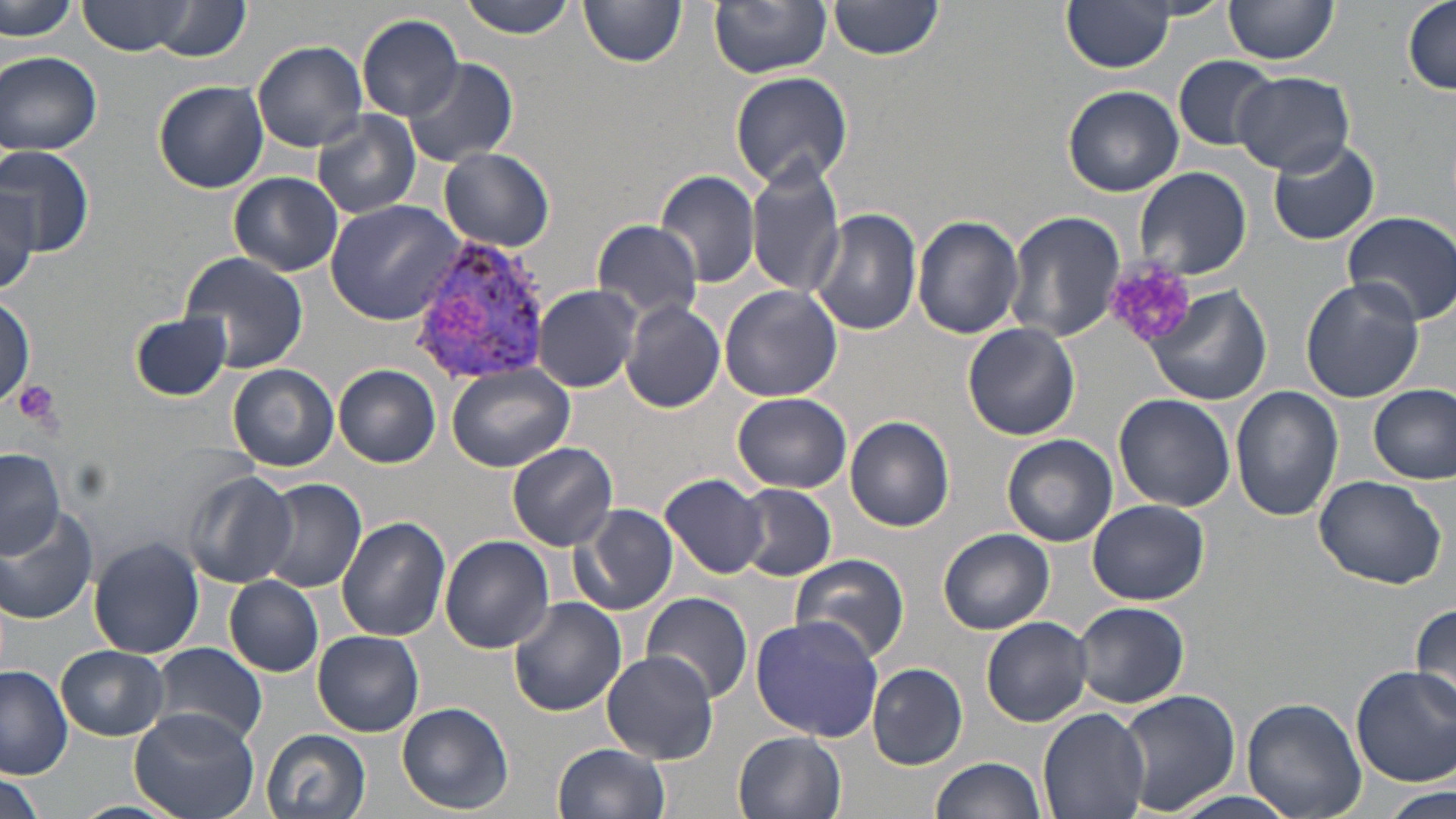

Summary:
  - Coordinate format: approximate bounding boxes as named x1/y1/x2/y2 corners in pixels
  - Uninfected red blood cell locations: (x1=79, y1=0, x2=197, y2=55), (x1=460, y1=0, x2=581, y2=40), (x1=827, y1=0, x2=946, y2=59), (x1=1063, y1=0, x2=1173, y2=72), (x1=1404, y1=0, x2=1456, y2=97), (x1=579, y1=1, x2=686, y2=69), (x1=709, y1=1, x2=831, y2=77), (x1=1222, y1=1, x2=1340, y2=67), (x1=3, y1=2, x2=77, y2=46), (x1=143, y1=2, x2=251, y2=62), (x1=358, y1=14, x2=465, y2=120), (x1=253, y1=40, x2=369, y2=151), (x1=0, y1=51, x2=101, y2=157), (x1=1173, y1=54, x2=1277, y2=152), (x1=401, y1=58, x2=518, y2=169), (x1=730, y1=70, x2=854, y2=190), (x1=1234, y1=72, x2=1355, y2=175), (x1=153, y1=80, x2=269, y2=193), (x1=1063, y1=85, x2=1183, y2=196), (x1=313, y1=113, x2=422, y2=219), (x1=1268, y1=138, x2=1380, y2=245), (x1=0, y1=145, x2=96, y2=257), (x1=440, y1=147, x2=556, y2=252), (x1=747, y1=155, x2=845, y2=298), (x1=1134, y1=166, x2=1251, y2=279), (x1=656, y1=169, x2=759, y2=288), (x1=227, y1=172, x2=343, y2=276), (x1=0, y1=181, x2=42, y2=291), (x1=324, y1=197, x2=468, y2=323), (x1=1006, y1=207, x2=1127, y2=344), (x1=810, y1=208, x2=922, y2=336), (x1=1341, y1=210, x2=1456, y2=326), (x1=915, y1=215, x2=1024, y2=338), (x1=593, y1=219, x2=703, y2=321), (x1=181, y1=252, x2=308, y2=373), (x1=1301, y1=278, x2=1426, y2=404), (x1=534, y1=283, x2=642, y2=392), (x1=718, y1=283, x2=843, y2=402), (x1=1145, y1=283, x2=1273, y2=407), (x1=0, y1=296, x2=34, y2=406), (x1=621, y1=300, x2=725, y2=412), (x1=133, y1=313, x2=231, y2=400), (x1=963, y1=323, x2=1079, y2=440), (x1=228, y1=364, x2=339, y2=471), (x1=335, y1=364, x2=441, y2=468), (x1=446, y1=367, x2=574, y2=473), (x1=1370, y1=385, x2=1454, y2=484), (x1=1230, y1=386, x2=1343, y2=522), (x1=732, y1=393, x2=851, y2=492), (x1=1113, y1=394, x2=1236, y2=512), (x1=845, y1=415, x2=955, y2=532), (x1=1003, y1=434, x2=1117, y2=547), (x1=507, y1=441, x2=619, y2=548), (x1=0, y1=450, x2=66, y2=554), (x1=183, y1=471, x2=297, y2=587), (x1=662, y1=473, x2=771, y2=578), (x1=1312, y1=473, x2=1448, y2=589), (x1=256, y1=477, x2=367, y2=593), (x1=734, y1=484, x2=837, y2=580), (x1=286, y1=486, x2=438, y2=622), (x1=1088, y1=500, x2=1209, y2=604), (x1=570, y1=502, x2=678, y2=617), (x1=0, y1=505, x2=99, y2=624), (x1=336, y1=516, x2=451, y2=643), (x1=938, y1=527, x2=1054, y2=635), (x1=440, y1=534, x2=556, y2=653), (x1=88, y1=536, x2=205, y2=659), (x1=790, y1=553, x2=910, y2=664), (x1=225, y1=577, x2=324, y2=678), (x1=641, y1=592, x2=752, y2=708), (x1=509, y1=598, x2=628, y2=717), (x1=1410, y1=599, x2=1456, y2=717), (x1=1073, y1=601, x2=1189, y2=709), (x1=749, y1=616, x2=883, y2=743), (x1=980, y1=616, x2=1094, y2=727), (x1=314, y1=631, x2=424, y2=736), (x1=150, y1=642, x2=267, y2=749), (x1=57, y1=645, x2=169, y2=741), (x1=601, y1=651, x2=721, y2=764), (x1=867, y1=662, x2=969, y2=770), (x1=0, y1=666, x2=74, y2=779), (x1=1349, y1=666, x2=1455, y2=788), (x1=1112, y1=687, x2=1239, y2=818), (x1=1242, y1=697, x2=1364, y2=819), (x1=397, y1=701, x2=514, y2=814), (x1=131, y1=706, x2=258, y2=819), (x1=1039, y1=708, x2=1151, y2=819), (x1=261, y1=728, x2=371, y2=819), (x1=734, y1=731, x2=847, y2=819), (x1=553, y1=741, x2=671, y2=819), (x1=932, y1=756, x2=1046, y2=819), (x1=0, y1=769, x2=44, y2=819), (x1=1382, y1=785, x2=1452, y2=819), (x1=1155, y1=791, x2=1310, y2=819), (x1=69, y1=800, x2=183, y2=819)
  - Platelet locations: (x1=1103, y1=260, x2=1200, y2=350), (x1=12, y1=381, x2=63, y2=432)
  - Plasmodium vivax-infected red blood cell locations: (x1=407, y1=232, x2=551, y2=387)
  - Slide-level diagnosis: Plasmodium vivax
  - Stain: May-Grünwald-Giemsa
  - Magnification: 1000x
  - Image size: 1456×819 pixels
  - Preparation: thin blood film
  - Modality: optical microscopy
  - Field of view: one of a larger specimen